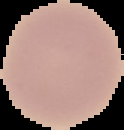
Summary:
  - Image type: cell region segmented out of the field of view; surrounding area masked to black
  - Malaria status: uninfected
  - Preparation: thin blood film
  - Image size: 124×130 pixels